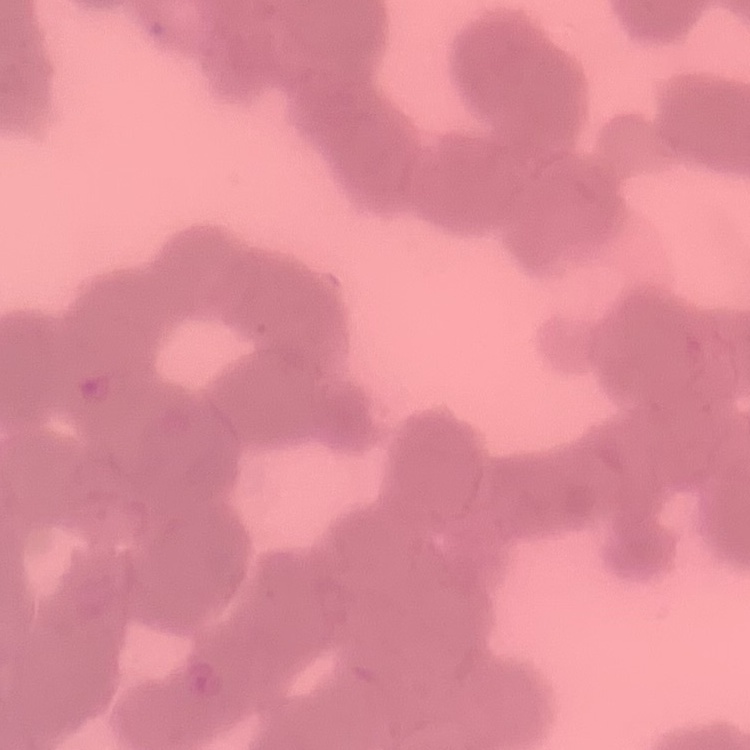 The red blood cells exhibit rouleaux formation. Square crop of a larger photomicrograph. Thin blood film. Field's or Giemsa stain.